Name the parasite shown.
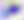
Toxoplasma gondii.

magnification = 400x
modality = micrograph